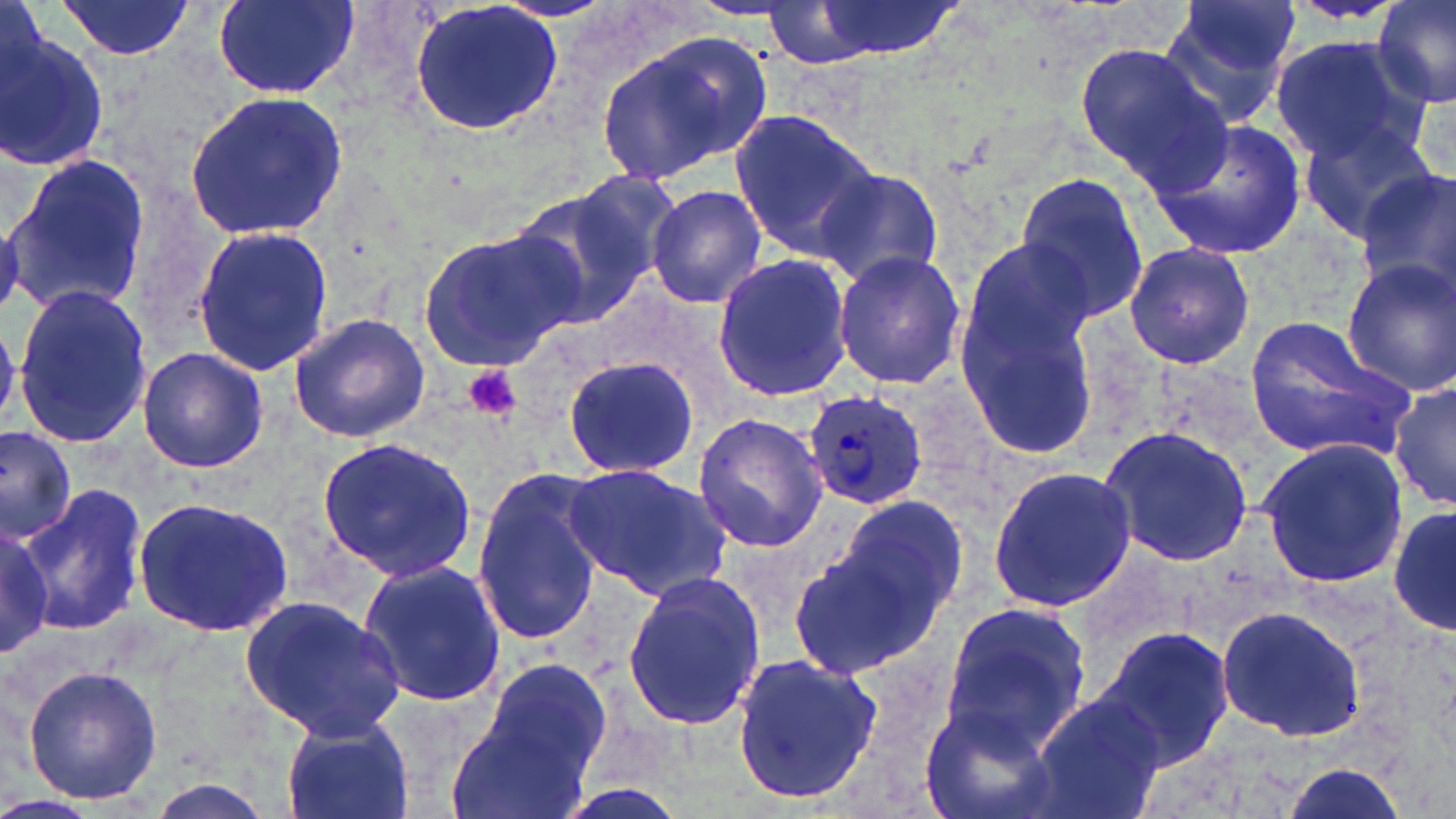
{
  "slide_level_diagnosis": "Plasmodium ovale",
  "stain": "May-Grünwald-Giemsa",
  "image_size": "1456×819 pixels",
  "platelet_locations": "approximate bounding boxes as (x1,y1)-(x2,y2) corner pairs in pixels: (460,364)-(523,423)",
  "field_of_view": "one of a larger specimen",
  "uninfected_red_blood_cell_locations": "approximate bounding boxes as (x1,y1)-(x2,y2) corner pairs in pixels: (56,0)-(195,59), (210,0)-(362,100), (408,0)-(564,138), (1164,0)-(1302,122), (1373,0)-(1456,110), (799,1)-(965,61), (759,4)-(890,70), (1,24)-(109,175), (596,33)-(769,186), (1272,35)-(1424,161), (1075,40)-(1230,188), (185,92)-(348,237), (731,111)-(883,260), (1152,117)-(1306,261), (1297,117)-(1444,244), (4,151)-(151,315), (814,168)-(949,289), (1015,168)-(1152,327), (558,169)-(687,304), (1354,171)-(1456,298), (645,184)-(768,311), (501,189)-(649,330), (191,223)-(333,378), (417,230)-(583,372), (959,240)-(1099,372), (1123,241)-(1255,371), (833,249)-(966,389), (711,254)-(852,403), (1341,257)-(1456,394), (12,285)-(154,447), (959,300)-(1101,459), (286,312)-(430,443), (1243,317)-(1415,461), (137,346)-(268,472), (560,355)-(702,478), (1390,380)-(1456,511), (692,412)-(828,555), (0,424)-(79,548), (1099,425)-(1255,567), (317,438)-(477,582), (1257,440)-(1409,588), (563,463)-(733,599), (987,463)-(1136,613), (471,467)-(610,646), (23,482)-(147,634), (130,493)-(298,637), (1388,499)-(1456,639), (797,501)-(965,676), (0,517)-(54,659), (359,559)-(506,708), (622,571)-(766,733), (239,593)-(406,741), (939,602)-(1093,753), (1215,604)-(1367,744), (1097,626)-(1236,766), (729,651)-(885,806), (470,656)-(615,797), (21,665)-(164,806), (1027,691)-(1167,819), (920,704)-(1062,819), (446,711)-(592,819), (280,713)-(415,819), (1274,762)-(1415,819)",
  "magnification": "1000x",
  "plasmodium_ovale_infected_red_blood_cell_locations": "approximate bounding boxes as (x1,y1)-(x2,y2) corner pairs in pixels: (805,392)-(928,511)",
  "preparation": "thin blood smear",
  "modality": "optical microscopy"
}